Outline each Plasmodium falciparum-infected red blood cell.
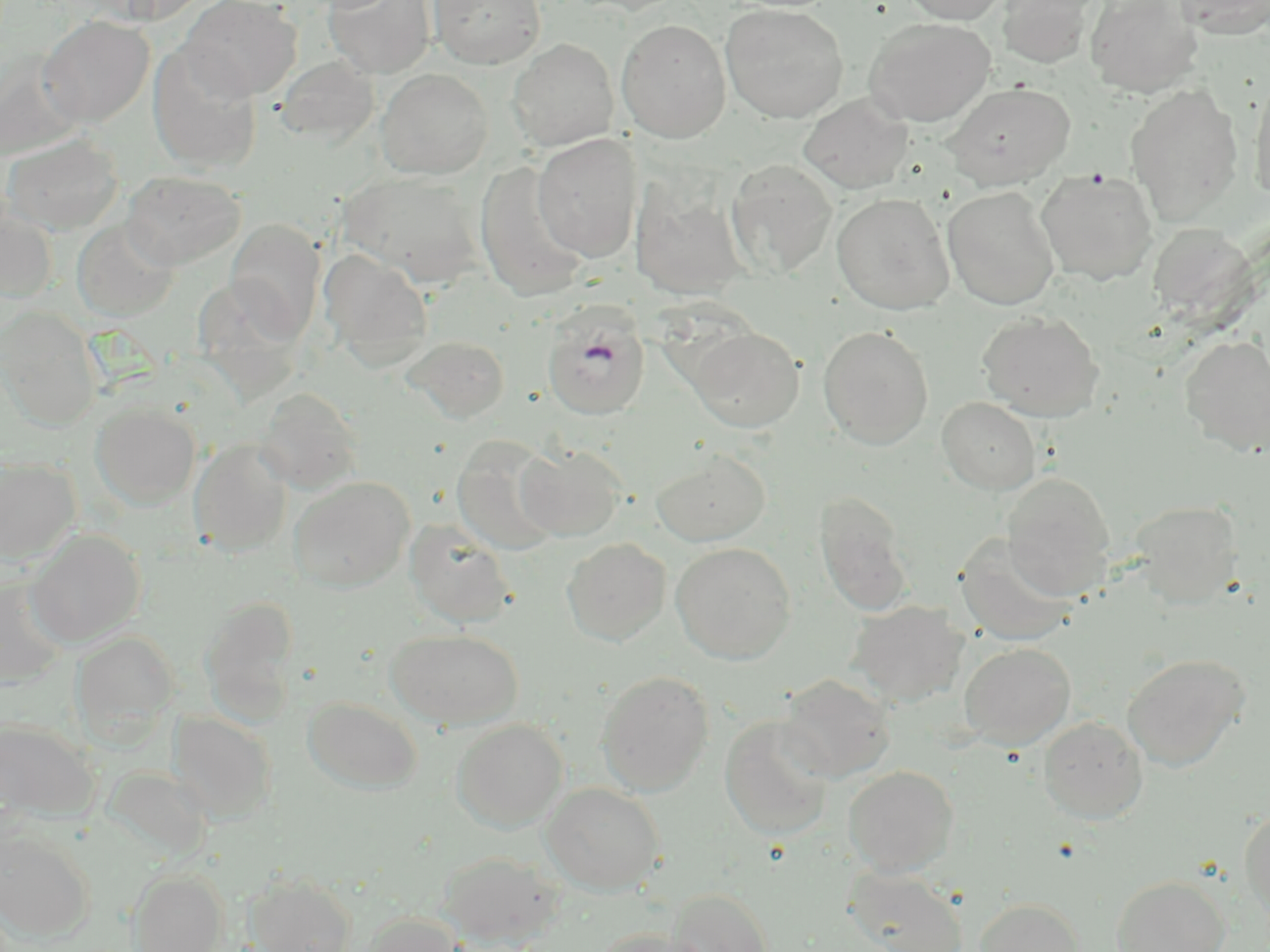
Approximate bounding boxes as (x1,y1)-(x2,y2) corner pairs in pixels.
Plasmodium falciparum-infected red blood cells: (542,305)-(650,420).

Summary:
  - Uninfected red blood cell locations: (180,0)-(302,101), (324,0)-(436,78), (428,0)-(546,69), (567,0)-(690,16), (901,0)-(1011,25), (996,0)-(1100,68), (1084,0)-(1203,97), (1172,0)-(1270,39), (721,4)-(849,122), (38,15)-(155,127), (864,17)-(996,126), (616,18)-(731,143), (508,38)-(619,151), (148,43)-(262,174), (0,51)-(83,162), (277,55)-(379,146), (376,68)-(492,179), (1249,76)-(1270,203), (942,82)-(1076,189), (1126,83)-(1244,224), (798,95)-(913,194), (2,133)-(124,234), (532,133)-(642,262), (726,159)-(838,278), (475,161)-(588,301), (1035,168)-(1159,285), (122,170)-(245,269), (338,171)-(486,287), (630,177)-(751,301), (941,186)-(1061,310), (831,192)-(955,314), (0,200)-(56,303), (72,219)-(179,321), (225,219)-(325,341), (1146,224)-(1255,322), (319,248)-(433,365), (0,308)-(101,430), (977,311)-(1105,421), (689,325)-(805,432), (817,325)-(934,448), (401,335)-(511,423), (1179,335)-(1270,456), (256,387)-(364,494), (937,397)-(1041,494), (91,403)-(201,510), (451,435)-(565,556), (189,438)-(294,556), (517,444)-(627,540), (650,449)-(771,546), (0,457)-(81,564), (1002,472)-(1115,596), (289,476)-(415,592), (814,490)-(915,617), (1130,500)-(1243,607), (405,519)-(518,628), (26,529)-(146,647), (955,533)-(1078,646), (561,538)-(671,646), (671,542)-(797,664), (1,576)-(72,688), (200,595)-(301,723), (847,600)-(969,707), (386,628)-(523,728), (72,632)-(179,745), (959,642)-(1076,749), (1123,653)-(1249,771), (596,670)-(715,796), (779,674)-(895,782), (303,696)-(423,794), (167,711)-(276,823), (720,716)-(835,840), (1038,716)-(1148,823), (452,718)-(568,831), (0,719)-(100,821), (843,765)-(959,876), (541,782)-(664,894), (1240,806)-(1270,924), (0,828)-(95,941), (439,849)-(565,949), (843,867)-(968,952), (128,869)-(228,952), (246,873)-(357,952), (1110,875)-(1231,952), (667,888)-(774,952), (975,897)-(1085,952), (361,913)-(467,952), (592,928)-(714,952)
  - Slide-level diagnosis: Plasmodium falciparum
  - Modality: light microscopy
  - Magnification: 1000x
  - Field of view: single
  - Preparation: thin blood film
  - Image size: 1270×952 pixels
  - Stain: May-Grünwald-Giemsa